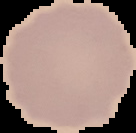

Summary:
  - Malaria status: uninfected
  - Image size: 136×133 pixels
  - Preparation: thin blood film
  - Image type: segmented cell region on a black background